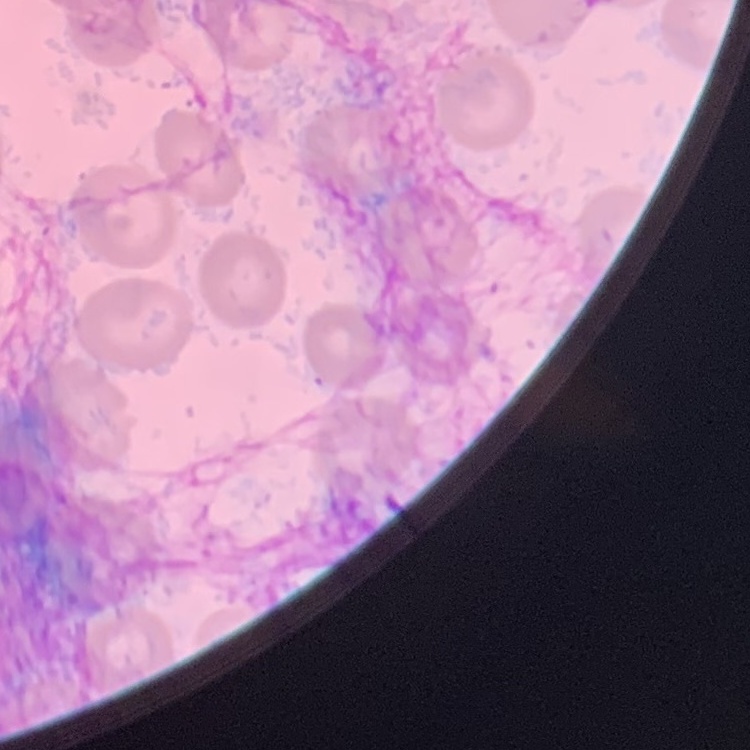

erythrocyte morphology = no rouleaux formation
image type = one tile cut from a larger photomicrograph
stain = Field's or Giemsa
preparation = thin blood film